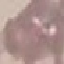

Summary:
  - Result: no malaria parasites detected
  - Image type: automatically extracted cell patch, resized to 64 × 64 pixels
  - Stain: Giemsa
  - Preparation: thin blood smear
  - Capture: smartphone through the microscope eyepiece